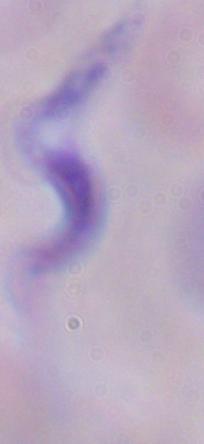
Summary:
  - Magnification: 1000x
  - Modality: photomicrograph
  - Identification: trypanosome